Identify the cell.
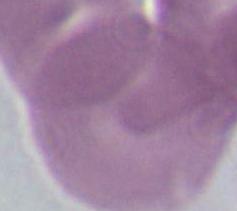
This is an erythrocyte.

Photomicrograph. Captured at 1000x magnification.